Point out cells.
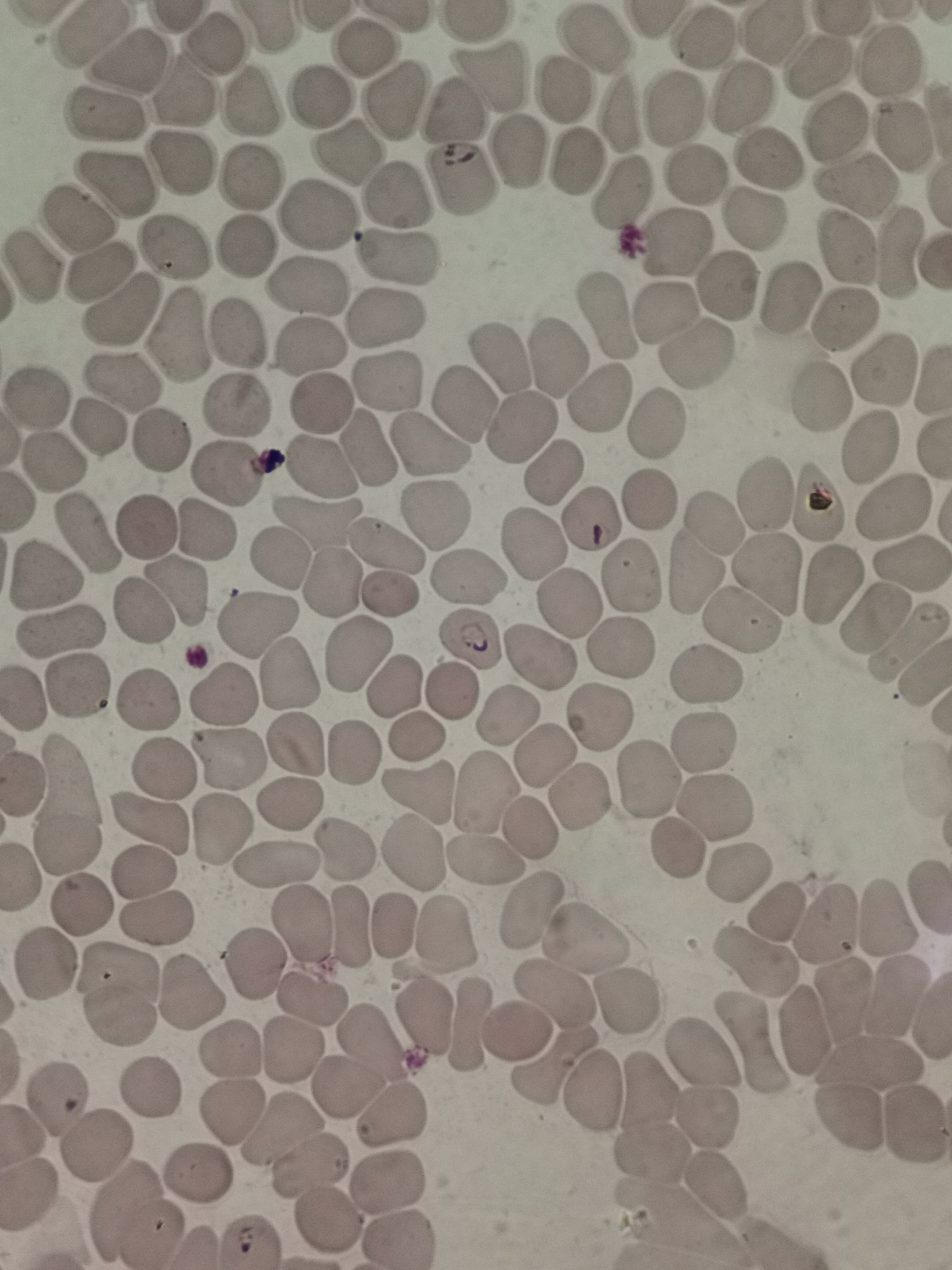
Approximate centers as (x, y) in pixels.
Cells: (84, 35), (775, 35), (703, 39), (593, 42), (212, 44), (358, 48), (129, 57), (888, 61), (819, 64), (489, 80), (185, 89), (318, 95), (398, 98), (741, 99), (252, 101), (681, 108), (452, 112), (104, 116), (622, 116), (839, 128), (898, 137), (515, 150), (344, 154), (776, 155), (577, 161), (178, 162), (695, 177), (108, 178), (246, 178), (860, 181), (458, 182), (624, 189), (395, 197), (756, 215), (313, 216), (74, 221), (679, 242), (242, 244), (173, 247), (848, 248), (896, 255), (399, 256), (30, 266), (97, 274), (729, 280), (304, 284), (789, 298), (113, 308), (670, 314), (389, 319), (607, 319), (845, 319), (175, 333), (233, 334), (312, 343), (697, 354), (560, 355), (500, 360), (878, 374), (118, 379), (392, 382), (822, 397), (35, 398), (600, 399), (319, 401), (461, 404), (236, 408), (97, 425), (523, 426), (654, 427), (163, 442), (426, 443), (875, 446), (370, 447), (54, 463), (322, 465), (226, 469), (551, 469), (767, 494), (650, 499), (819, 503), (897, 509), (438, 515), (591, 516), (713, 522), (315, 524), (148, 526), (203, 526), (87, 532), (386, 542), (534, 552), (274, 558), (908, 563), (696, 571), (770, 573), (46, 576), (629, 577), (828, 578), (465, 580), (331, 581), (390, 592), (175, 593), (572, 604), (140, 614), (870, 614), (257, 618), (745, 619), (63, 627), (471, 642), (904, 643), (354, 646), (623, 648), (540, 658), (288, 673), (705, 675), (78, 684), (392, 687), (220, 694), (452, 694), (147, 700), (598, 718), (510, 722), (415, 738), (295, 741), (701, 745), (356, 751), (550, 751), (227, 757), (161, 768), (71, 774), (651, 779), (23, 781), (483, 790), (420, 792), (577, 801), (287, 802), (714, 807), (152, 817), (221, 826), (527, 833), (72, 846), (680, 848), (345, 849), (407, 851), (486, 858), (279, 866), (739, 867), (147, 870), (84, 901), (776, 910), (530, 911), (886, 915), (157, 920), (307, 922), (827, 923), (351, 927), (392, 927), (448, 930), (581, 938), (754, 960), (48, 964), (256, 966), (118, 976), (191, 991), (555, 995), (844, 996), (898, 996), (315, 998), (625, 999), (121, 1019), (426, 1020), (467, 1025), (518, 1032), (804, 1033), (752, 1042), (371, 1044), (233, 1049), (701, 1055), (870, 1064), (547, 1069), (151, 1083), (345, 1085), (593, 1090), (650, 1091), (59, 1097), (233, 1109), (708, 1111), (393, 1113), (851, 1116), (913, 1124), (278, 1133), (100, 1139), (655, 1151), (311, 1167), (194, 1175), (718, 1181), (390, 1184), (134, 1211), (328, 1216), (401, 1233).

field of view = single
image size = 952×1270 pixels
capture = smartphone through the microscope eyepiece
stain = Giemsa
preparation = thin smear